Name the cell type shown.
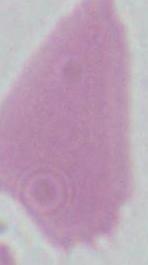

This is an erythrocyte.

Micrograph. 1000x magnification.